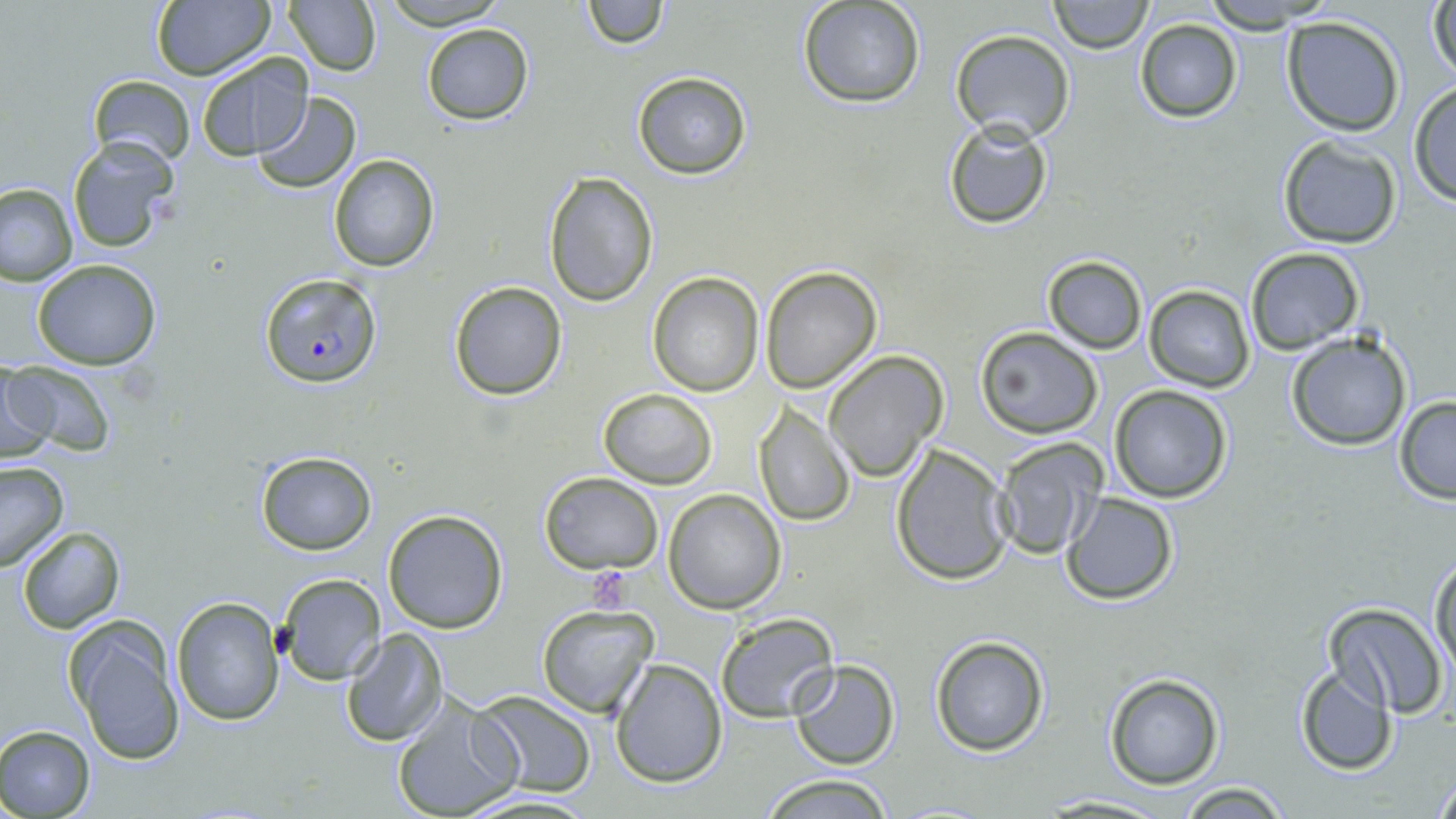
Approximate bounding boxes as named x1/y1/x2/y2 corners in pixels. Plasmodium falciparum-infected red blood cell locations: (x1=259, y1=272, x2=381, y2=388). Uninfected red blood cell locations: (x1=282, y1=0, x2=381, y2=75), (x1=377, y1=0, x2=512, y2=29), (x1=580, y1=0, x2=666, y2=50), (x1=1047, y1=0, x2=1153, y2=53), (x1=1198, y1=0, x2=1334, y2=32), (x1=1427, y1=0, x2=1456, y2=86), (x1=150, y1=1, x2=275, y2=82), (x1=796, y1=1, x2=926, y2=108), (x1=1280, y1=17, x2=1404, y2=136), (x1=1134, y1=19, x2=1244, y2=122), (x1=421, y1=23, x2=533, y2=126), (x1=950, y1=30, x2=1074, y2=142), (x1=196, y1=52, x2=312, y2=160), (x1=632, y1=70, x2=753, y2=181), (x1=86, y1=75, x2=196, y2=167), (x1=1408, y1=83, x2=1456, y2=207), (x1=251, y1=93, x2=360, y2=194), (x1=943, y1=119, x2=1055, y2=230), (x1=67, y1=135, x2=179, y2=252), (x1=1277, y1=135, x2=1402, y2=249), (x1=329, y1=154, x2=442, y2=272), (x1=544, y1=172, x2=659, y2=307), (x1=0, y1=182, x2=77, y2=285), (x1=1245, y1=247, x2=1363, y2=354), (x1=1042, y1=254, x2=1148, y2=354), (x1=31, y1=259, x2=162, y2=370), (x1=760, y1=265, x2=884, y2=393), (x1=647, y1=274, x2=764, y2=396), (x1=446, y1=280, x2=569, y2=402), (x1=1145, y1=285, x2=1254, y2=392), (x1=975, y1=328, x2=1104, y2=439), (x1=1285, y1=331, x2=1411, y2=452), (x1=824, y1=350, x2=949, y2=481), (x1=0, y1=363, x2=57, y2=464), (x1=10, y1=363, x2=110, y2=455), (x1=1107, y1=384, x2=1235, y2=503), (x1=598, y1=387, x2=717, y2=489), (x1=1393, y1=396, x2=1456, y2=503), (x1=753, y1=404, x2=855, y2=527), (x1=990, y1=436, x2=1109, y2=561), (x1=890, y1=442, x2=1016, y2=585), (x1=255, y1=451, x2=377, y2=555), (x1=0, y1=461, x2=70, y2=571), (x1=539, y1=472, x2=664, y2=574), (x1=662, y1=490, x2=786, y2=612), (x1=1062, y1=492, x2=1179, y2=605), (x1=382, y1=509, x2=508, y2=632), (x1=16, y1=526, x2=125, y2=634), (x1=1430, y1=554, x2=1456, y2=682), (x1=276, y1=573, x2=387, y2=684), (x1=171, y1=597, x2=283, y2=723), (x1=1323, y1=602, x2=1448, y2=718), (x1=535, y1=605, x2=656, y2=717), (x1=715, y1=612, x2=840, y2=723), (x1=64, y1=617, x2=187, y2=767), (x1=340, y1=629, x2=449, y2=747), (x1=929, y1=635, x2=1051, y2=756), (x1=609, y1=659, x2=725, y2=788), (x1=790, y1=661, x2=901, y2=768), (x1=1293, y1=666, x2=1400, y2=777), (x1=1102, y1=674, x2=1224, y2=790), (x1=470, y1=692, x2=598, y2=797), (x1=392, y1=695, x2=523, y2=819), (x1=0, y1=726, x2=96, y2=818), (x1=1430, y1=766, x2=1455, y2=819), (x1=756, y1=771, x2=896, y2=818), (x1=1174, y1=781, x2=1293, y2=818), (x1=1038, y1=794, x2=1175, y2=817). Platelet locations: (x1=585, y1=567, x2=636, y2=611). Slide-level diagnosis: Plasmodium falciparum. Captured at 1000x magnification. Image is 1456×819 pixels. One field of a larger specimen. May-Grünwald-Giemsa stain. Optical microscopy. Thin blood smear.